Point out each Plasmodium parasite.
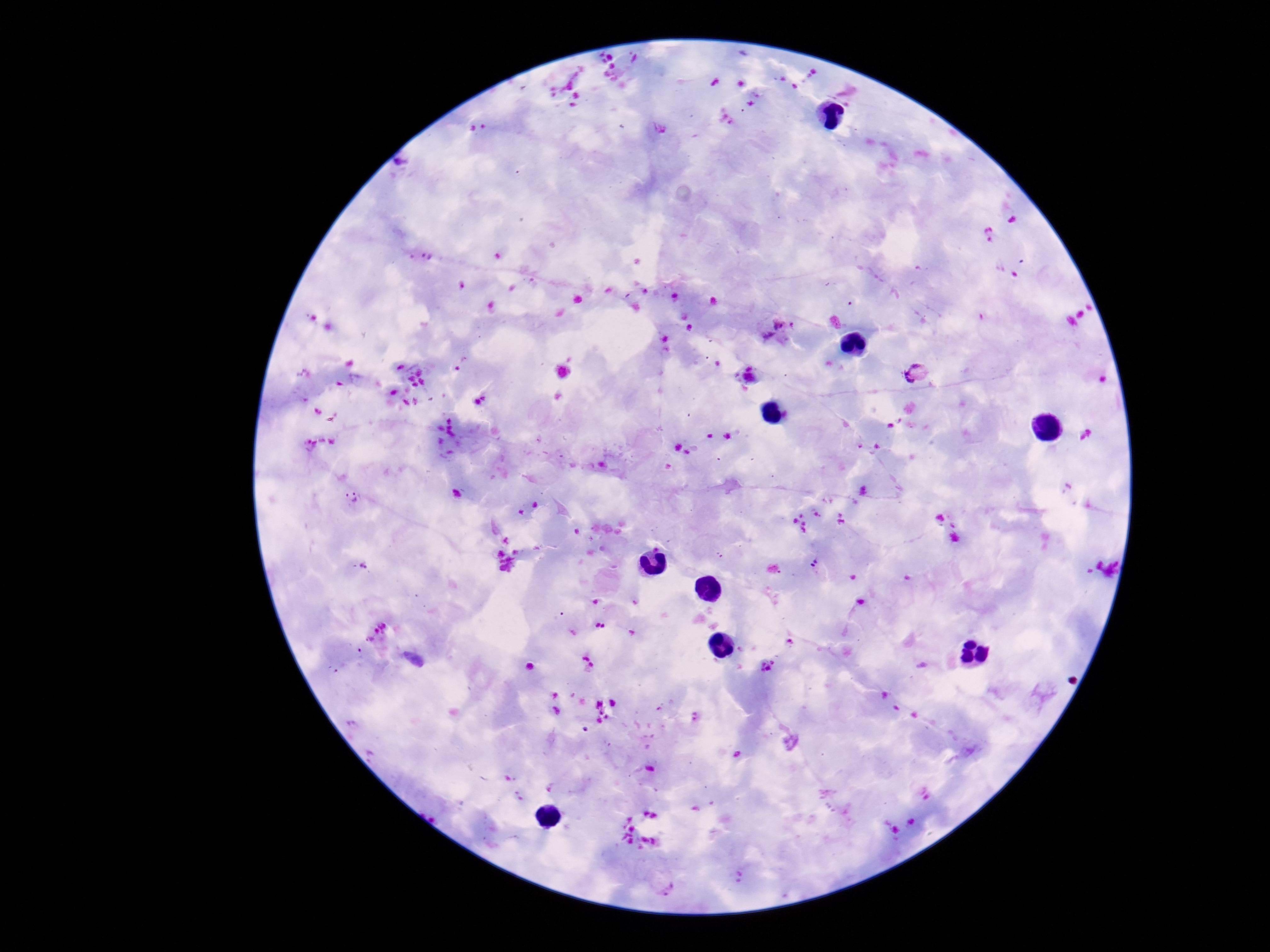
Approximate object centers, in pixels from the top-left corner.
Plasmodium parasites: (x=1013, y=218), (x=990, y=234), (x=777, y=328), (x=917, y=372), (x=352, y=496), (x=363, y=564), (x=819, y=569), (x=381, y=626), (x=369, y=641), (x=662, y=882).

magnification: 100x
preparation: thick peripheral-blood smear
stain: Giemsa
field_of_view: one from this slide
image_size: 1270×952 pixels
patient_malaria_status: positive
capture: smartphone camera through the microscope eyepiece